Outline each blood parasite and name the species.
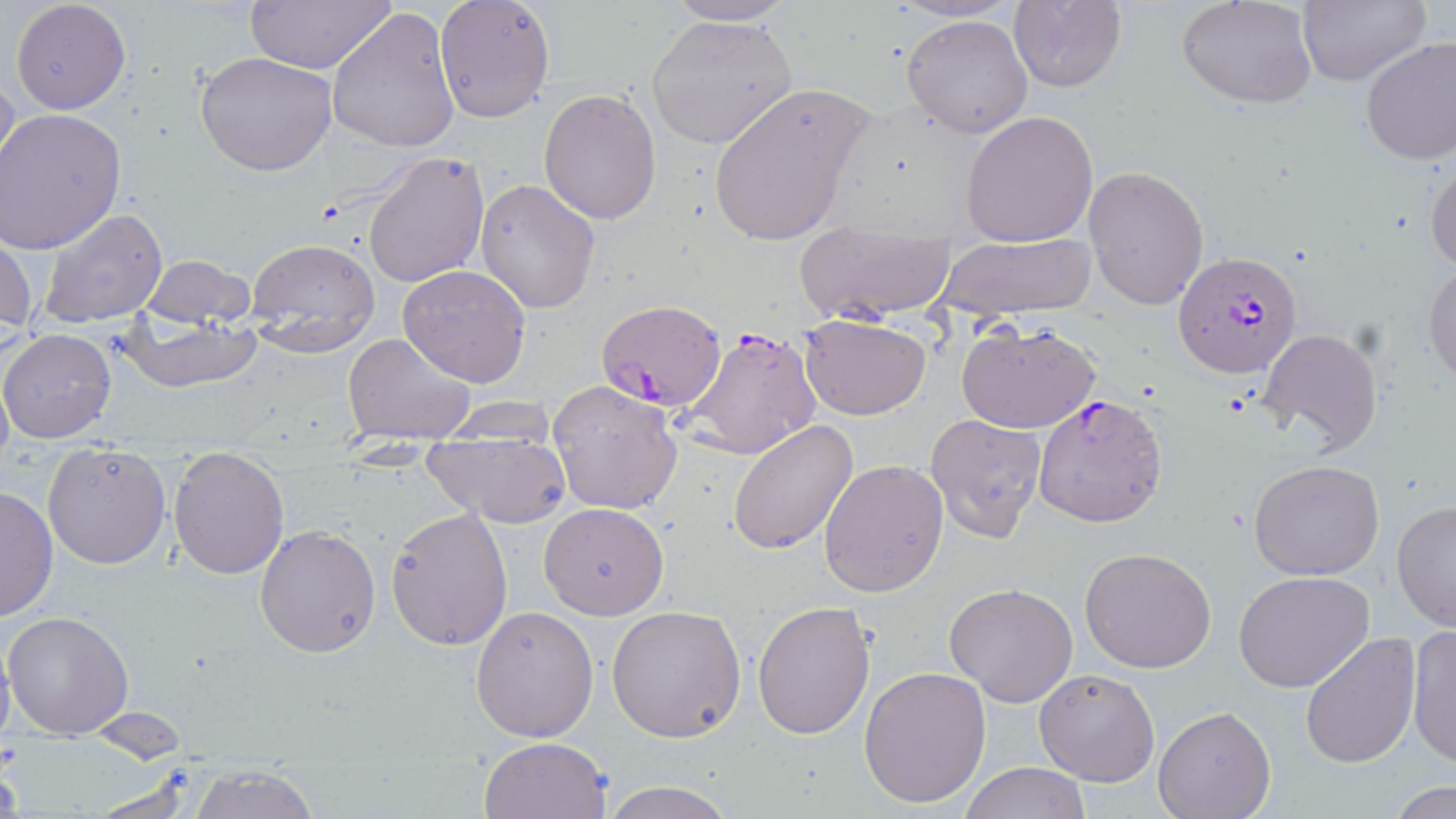

Approximate bounding boxes as (x1,y1)-(x2,y2) corner pairs in pixels.
Plasmodium falciparum-infected red blood cells: (1174,248)-(1303,380), (595,298)-(728,411), (682,323)-(824,458), (1033,393)-(1168,528).
No Plasmodium ovale, Plasmodium malariae, Plasmodium vivax, Babesia divergens, or Trypanosoma brucei observed.

slide-level diagnosis = Plasmodium falciparum
magnification = 1000x
image size = 1456×819 pixels
preparation = thin blood film
modality = light microscopy
stain = May-Grünwald-Giemsa
field of view = single
uninfected red blood cell locations = approximate bounding boxes as (x1,y1)-(x2,y2) corner pairs in pixels: (246,0)-(394,74), (434,0)-(556,124), (663,0)-(796,25), (1178,0)-(1317,109), (10,1)-(132,115), (1007,1)-(1126,92), (1296,1)-(1428,87), (327,8)-(460,154), (901,13)-(1034,139), (646,14)-(796,150), (1359,36)-(1456,167), (195,50)-(339,176), (0,69)-(20,185), (708,80)-(874,248), (539,89)-(661,224), (0,108)-(127,254), (961,111)-(1100,247), (364,151)-(491,288), (1427,158)-(1456,274), (1083,164)-(1210,309), (475,178)-(601,313), (36,208)-(168,330), (792,221)-(958,325), (0,225)-(39,347), (933,232)-(1098,322), (245,237)-(380,357), (140,255)-(254,328), (1424,263)-(1456,387), (399,265)-(532,387), (120,309)-(260,391), (798,314)-(932,421), (956,321)-(1102,433), (1,328)-(116,443), (1256,328)-(1383,459), (344,330)-(476,442), (0,365)-(13,475), (547,381)-(684,514), (442,396)-(558,444), (924,412)-(1047,542), (728,421)-(859,555), (422,438)-(572,527), (43,440)-(173,570), (168,450)-(290,579), (819,458)-(948,597), (1249,460)-(1385,582), (0,480)-(58,624), (1392,501)-(1456,632), (538,502)-(669,619), (384,508)-(512,651), (255,524)-(381,658), (1080,547)-(1217,673), (1233,571)-(1375,693), (944,582)-(1079,707), (753,602)-(875,740), (606,605)-(746,742), (470,606)-(601,742), (2,611)-(133,739), (1405,625)-(1456,769), (0,633)-(16,753), (1298,633)-(1420,768), (858,666)-(991,809), (1034,667)-(1160,787), (1153,706)-(1275,819), (478,736)-(613,819), (960,761)-(1090,818), (189,765)-(319,819), (600,781)-(734,819), (1384,782)-(1454,819)